Identify the preparation type.
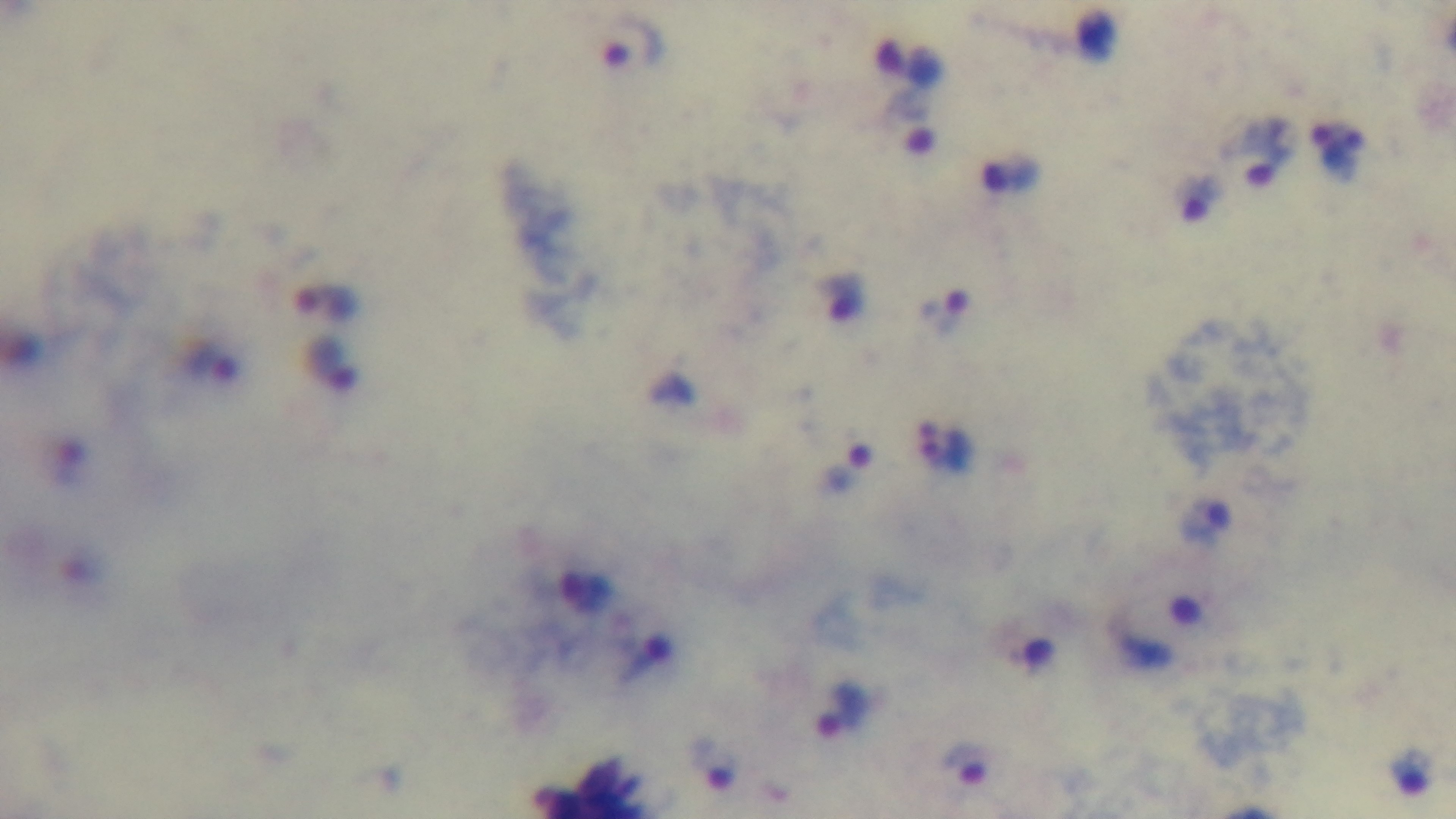
Thick.

Summary:
  - Field of view: single
  - Objective: 100x oil immersion
  - Stain: Giemsa
  - Modality: light microscopy
  - Malaria status: positive
  - Capture: mounted 4K digital camera